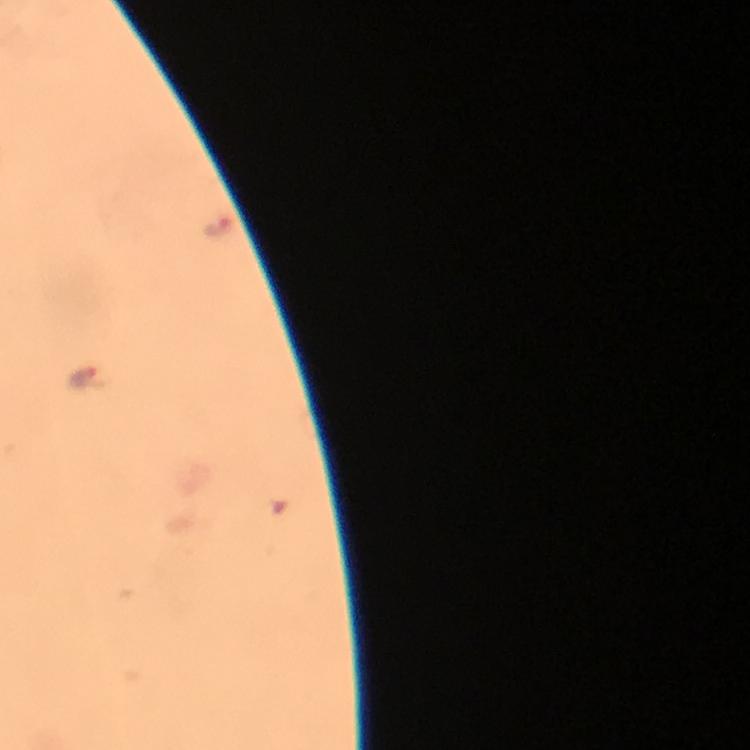

image_size: 750×750 pixels
preparation: thick smear
capture: smartphone photograph through a microscope
magnification: 100x
stain: Giemsa
immersion_oil: used
cropped_from: one field of view
plasmodium_parasite_locations: 'approximate object centers, in pixels from the top-left corner: (x=219, y=227), (x=84, y=375)'
context: from a malaria diagnostic workup